Report the malaria status of this cell.
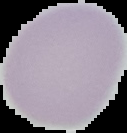
Uninfected.

Image is 127×133 pixels. Segmented cell region on a black background. From a thin blood smear.